Report the malaria status of this cell.
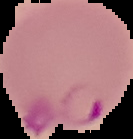
It is parasitized.

Image is 133×139 pixels. The area outside the segmented cell region is set to black. From a thin blood smear.